Locate and identify every blood parasite.
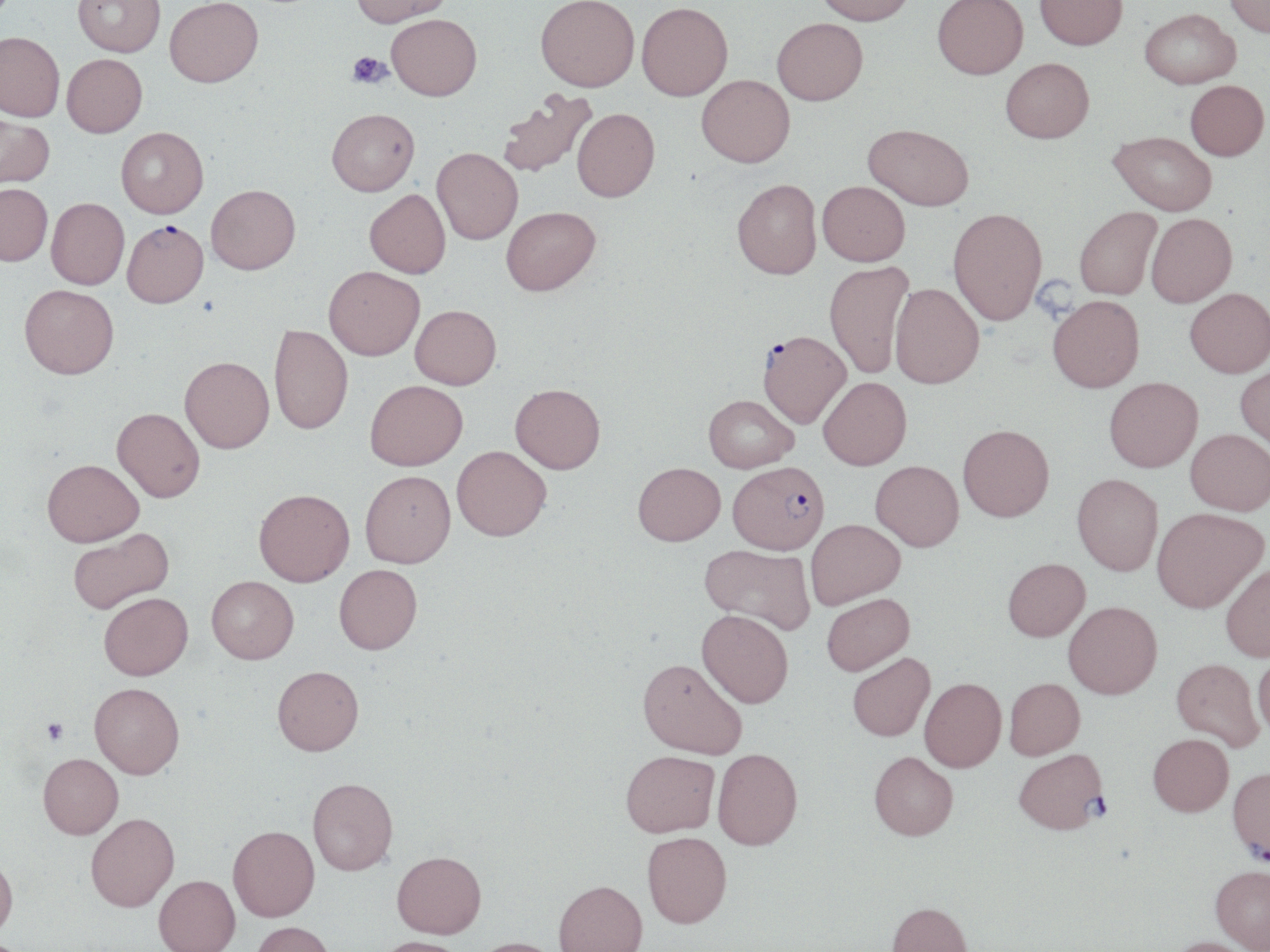

Approximate bounding boxes as (x1,y1)-(x2,y2) corner pairs in pixels.
Plasmodium falciparum-infected red blood cells: (122,224)-(209,312), (757,334)-(851,431), (728,462)-(829,555), (1014,748)-(1107,835), (1228,766)-(1270,862).
No Plasmodium ovale, Plasmodium malariae, Plasmodium vivax, Babesia divergens, or Trypanosoma brucei observed.

Platelet locations: (347,51)-(391,89), (42,718)-(69,745). Uninfected red blood cell locations: (72,0)-(165,60), (352,0)-(453,31), (535,0)-(639,96), (814,0)-(916,29), (932,0)-(1028,84), (1034,0)-(1127,54), (1224,0)-(1270,41), (165,1)-(264,92), (636,6)-(733,105), (1139,13)-(1241,92), (387,19)-(482,105), (772,22)-(868,110), (0,36)-(64,125), (62,57)-(147,141), (1001,62)-(1094,148), (696,78)-(795,172), (1185,84)-(1268,164), (497,89)-(599,180), (572,112)-(660,206), (327,113)-(420,200), (0,117)-(54,191), (862,128)-(973,215), (116,131)-(209,222), (1108,134)-(1216,219), (432,151)-(523,247), (731,183)-(823,284), (817,185)-(909,270), (0,186)-(51,270), (206,189)-(301,278), (364,192)-(450,281), (46,200)-(129,292), (1075,209)-(1162,302), (502,211)-(601,300), (948,212)-(1047,330), (1146,216)-(1237,311), (823,262)-(915,381), (323,270)-(424,364), (890,286)-(984,393), (18,288)-(119,384), (1185,292)-(1270,382), (1048,299)-(1144,397), (410,309)-(501,392), (269,327)-(353,437), (179,360)-(275,457), (1235,366)-(1270,455), (1104,380)-(1203,476), (819,381)-(911,472), (365,382)-(468,472), (510,385)-(605,474), (704,398)-(798,474), (112,411)-(204,503), (959,426)-(1055,524), (1185,430)-(1270,518), (452,445)-(552,540), (42,460)-(144,549), (870,461)-(964,552), (633,462)-(725,546), (360,470)-(456,568), (1071,474)-(1162,576), (254,489)-(355,588), (1152,507)-(1268,613), (806,519)-(905,608), (68,529)-(175,614), (700,544)-(815,634), (1003,558)-(1090,641), (1221,561)-(1270,662), (334,564)-(422,654), (207,575)-(298,664), (99,592)-(193,681), (822,593)-(914,675), (1063,601)-(1162,699), (696,609)-(793,707), (847,652)-(935,741), (1253,654)-(1270,740), (638,657)-(747,758), (1171,658)-(1263,751), (272,666)-(364,756), (919,677)-(1006,773), (1004,678)-(1085,760), (89,682)-(184,779), (1148,733)-(1233,816), (712,747)-(803,849), (621,751)-(719,836), (869,751)-(958,840), (38,753)-(123,839), (307,778)-(398,875), (86,812)-(180,913), (228,826)-(320,923), (642,831)-(732,928), (392,850)-(486,939), (0,854)-(18,940), (1210,865)-(1270,950), (154,875)-(239,952), (553,880)-(647,952), (886,902)-(973,952), (250,922)-(335,952), (373,936)-(468,952), (1165,936)-(1259,952), (470,937)-(564,952). Slide-level diagnosis: Plasmodium falciparum. One field of a larger specimen. 1000x magnification. May-Grünwald-Giemsa-stained preparation. Image is 1270×952 pixels. Optical microscopy. Thin blood film.